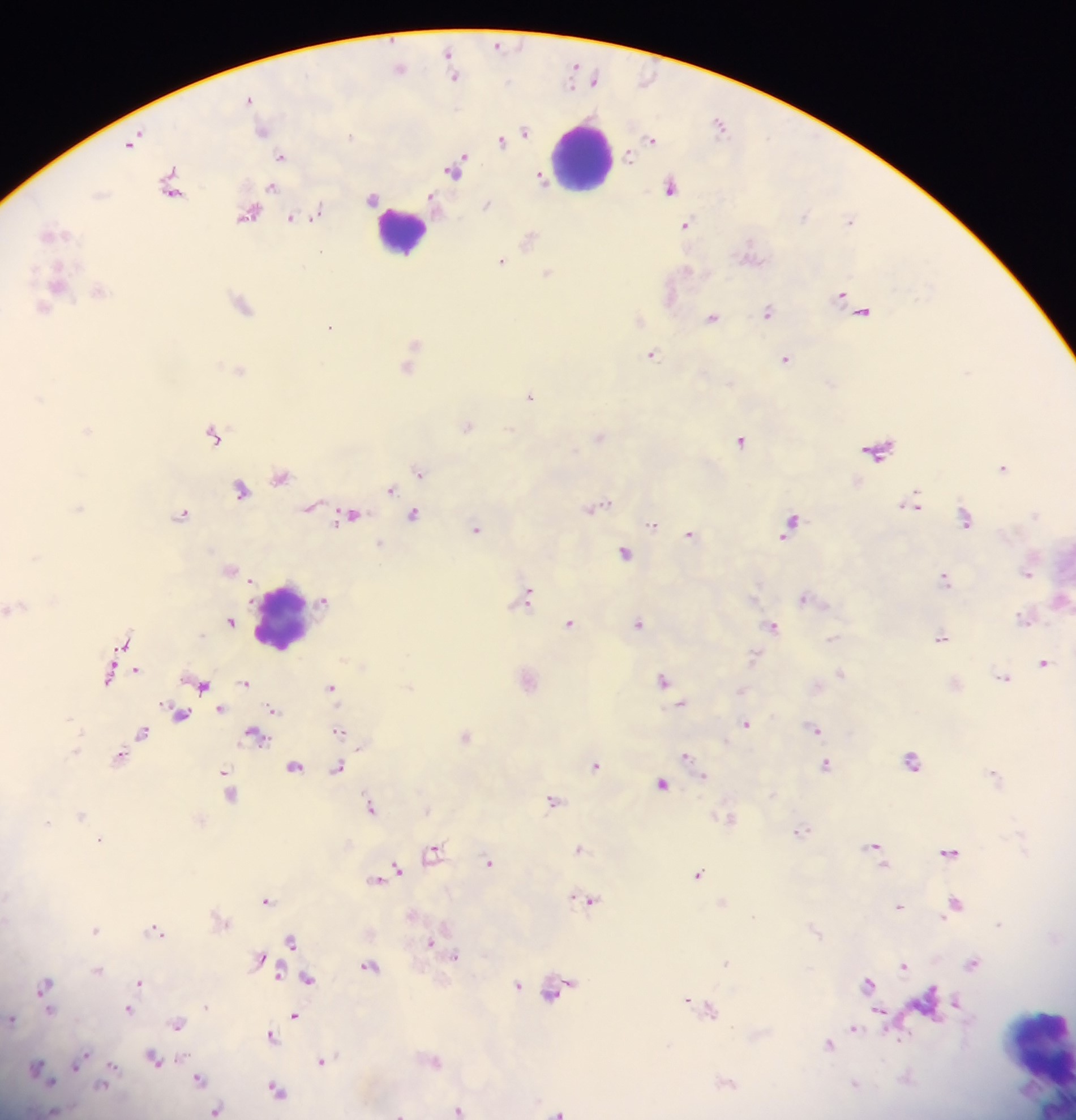
Approximate centers as (x, y) in pixels.
Summary:
  - Leukocyte locations: (581, 158), (401, 231), (284, 618), (1035, 1052)
  - Plasmodium parasite locations: (497, 46), (448, 53), (399, 68), (453, 75), (594, 80), (250, 99), (720, 124), (261, 130), (524, 131), (651, 138), (501, 139), (134, 140), (628, 155), (282, 156), (455, 168), (540, 178), (670, 186), (271, 187), (173, 189), (373, 198), (432, 200), (486, 205), (249, 213), (317, 213), (292, 218), (850, 219), (686, 225), (52, 233), (529, 238), (752, 253), (501, 261), (547, 273), (57, 282), (98, 290), (670, 294), (842, 295), (242, 304), (43, 307), (863, 311), (768, 312), (712, 317), (638, 319), (330, 327), (415, 343), (651, 354), (786, 359), (408, 366), (238, 370), (530, 397), (467, 425), (86, 430), (215, 435), (598, 437), (741, 440), (879, 450), (1003, 467), (419, 471), (281, 476), (241, 489), (391, 489), (914, 503), (310, 506), (79, 507), (596, 507), (182, 514), (413, 515), (350, 516), (965, 518), (791, 524), (652, 525), (477, 529), (690, 534), (380, 543), (624, 553), (229, 569), (1028, 571), (945, 578), (528, 595), (804, 598), (324, 599), (1060, 600), (10, 608), (1024, 617), (231, 621), (570, 623), (638, 624), (773, 626), (941, 637), (831, 639), (123, 643), (754, 656), (1044, 662), (136, 669), (840, 672), (108, 675), (528, 678), (1003, 678), (663, 680), (200, 682), (244, 682), (332, 687), (681, 705), (220, 709), (273, 709), (179, 713), (746, 723), (815, 727), (339, 730), (143, 731), (255, 734), (465, 737), (76, 752), (120, 756), (687, 756), (912, 761), (596, 765), (827, 765), (294, 766), (338, 768), (226, 772), (995, 776), (227, 780), (661, 783), (229, 792), (552, 801), (370, 807), (80, 814), (728, 818), (801, 831), (99, 839), (876, 846), (579, 848), (434, 851), (949, 851), (490, 862), (396, 870), (698, 874), (376, 879), (588, 899), (266, 900), (723, 903), (955, 904), (899, 906), (220, 918), (95, 929), (157, 930), (291, 940), (431, 944), (456, 957), (261, 958), (726, 962), (974, 962), (904, 965), (369, 966), (97, 970), (278, 974), (307, 978), (139, 982), (869, 983), (46, 985), (518, 985), (558, 988), (689, 1001), (928, 1002), (957, 1003), (206, 1005), (128, 1008), (710, 1008), (48, 1009), (879, 1012), (295, 1016), (11, 1018), (177, 1023), (854, 1029), (271, 1035), (830, 1044), (153, 1058), (79, 1060), (434, 1060), (322, 1061), (113, 1067), (37, 1069), (199, 1078), (726, 1082), (855, 1085), (101, 1086), (277, 1089), (215, 1110), (458, 1110), (51, 1111), (557, 1112), (400, 1113)
  - Preparation: thick blood smear
  - Capture: mobile-phone photograph through a microscope
  - Field of view: single
  - Image size: 1076×1120 pixels
  - Country: Ghana